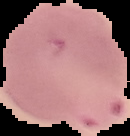 The area outside the segmented cell region is set to black. Result: Plasmodium parasites identified. Image is 130×136 pixels. From a thin blood smear.